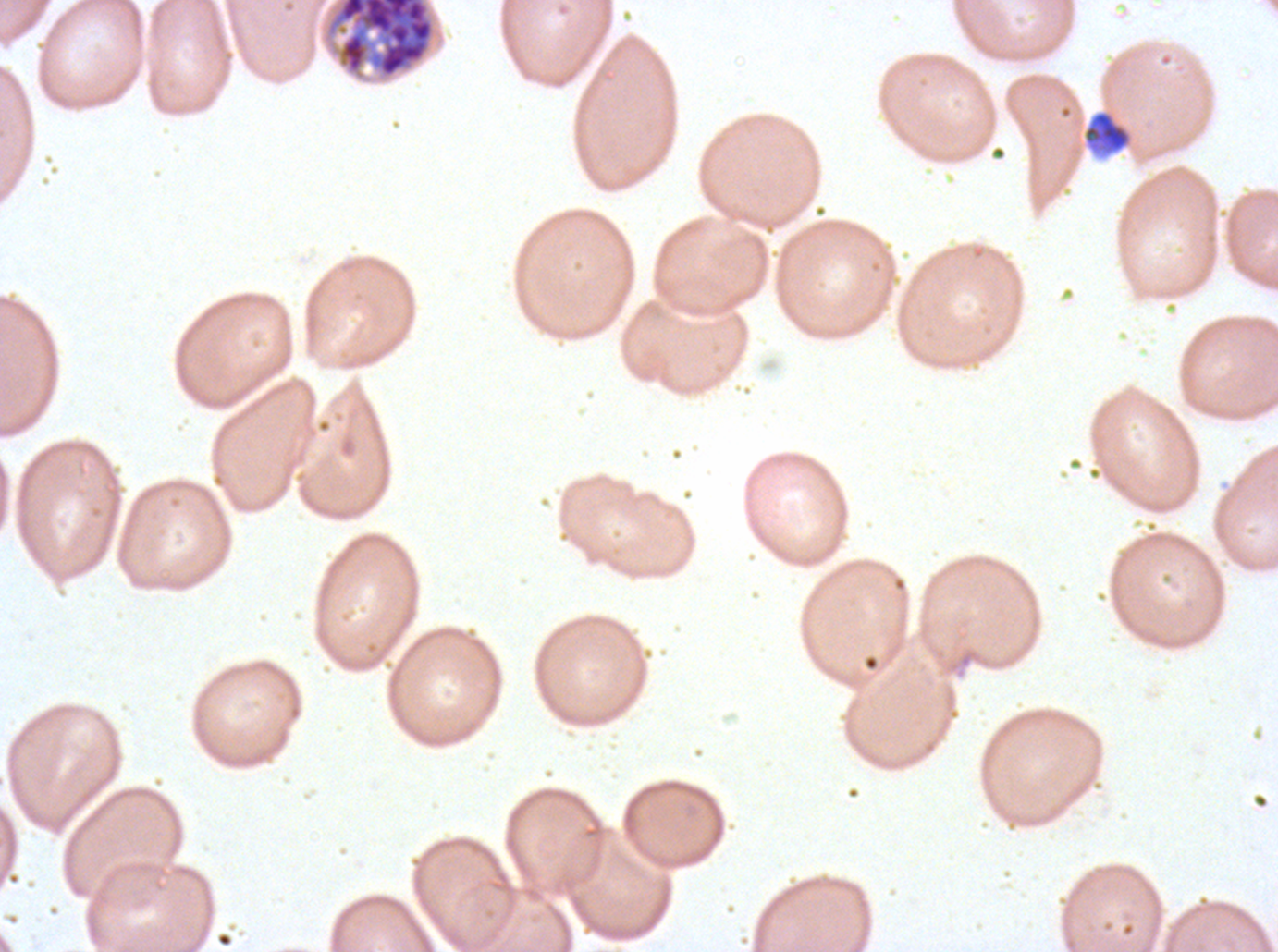
Approximate bounding boxes as (x1, y1, x2, y2) in pixels. Debris locations: (1082, 109, 1133, 156). Late schizont locations: (325, 0, 436, 79). Image is 1278×952 pixels. One sub-image of a larger composite. Thin blood smear. P. falciparum from a patient in The Gambia, cultured ex vivo for 24 to 48 hours. Giemsa-stained preparation.